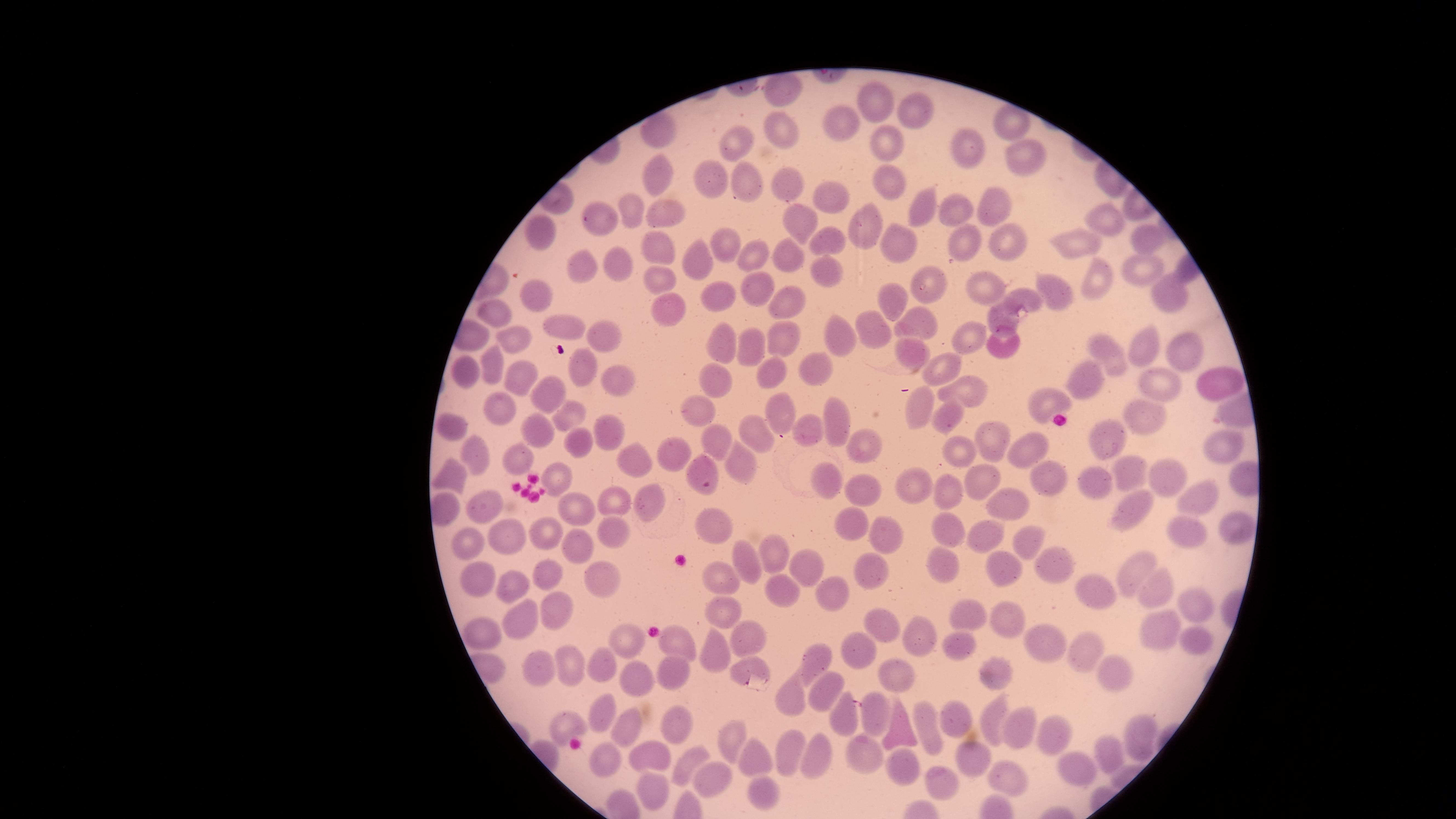

stain = Giemsa
field of view = single
visible region = circular
capture = smartphone photograph through the microscope eyepiece
uninfected RBCs = approximate marker points, in pixels from the top-left corner: (x=782, y=91), (x=879, y=101), (x=919, y=115), (x=838, y=119), (x=782, y=128), (x=655, y=132), (x=963, y=138), (x=733, y=140), (x=886, y=141), (x=1022, y=149), (x=653, y=174), (x=712, y=177), (x=888, y=178), (x=753, y=180), (x=785, y=180), (x=830, y=198), (x=994, y=202), (x=622, y=204), (x=916, y=205), (x=658, y=209), (x=795, y=212), (x=958, y=214), (x=1103, y=217), (x=598, y=219), (x=871, y=226), (x=830, y=230), (x=1145, y=235), (x=1010, y=236), (x=542, y=237), (x=896, y=238), (x=1078, y=240), (x=724, y=242), (x=958, y=246), (x=662, y=248), (x=702, y=254), (x=754, y=254), (x=794, y=254), (x=584, y=262), (x=830, y=262), (x=618, y=263), (x=1146, y=266), (x=664, y=278), (x=1103, y=278), (x=929, y=282), (x=982, y=286), (x=760, y=287), (x=1050, y=289), (x=894, y=291), (x=720, y=293), (x=545, y=294), (x=1179, y=298), (x=1026, y=299), (x=788, y=302), (x=664, y=304), (x=495, y=316), (x=917, y=316), (x=1004, y=319), (x=869, y=321), (x=568, y=326), (x=602, y=335), (x=963, y=336), (x=786, y=338), (x=516, y=340), (x=730, y=341), (x=841, y=341), (x=1004, y=342), (x=753, y=343), (x=908, y=344), (x=1182, y=345), (x=1149, y=349), (x=491, y=355), (x=1108, y=358), (x=579, y=365), (x=943, y=366), (x=822, y=367), (x=771, y=368), (x=469, y=374), (x=607, y=378), (x=1085, y=379), (x=1213, y=379), (x=718, y=383), (x=521, y=385), (x=969, y=386), (x=1159, y=386), (x=553, y=397), (x=1041, y=398), (x=780, y=405), (x=921, y=405), (x=699, y=406), (x=502, y=410), (x=572, y=414), (x=1141, y=418), (x=830, y=419), (x=948, y=421), (x=452, y=429), (x=537, y=430), (x=613, y=430), (x=813, y=432), (x=714, y=435), (x=994, y=435), (x=756, y=436), (x=1225, y=439), (x=579, y=441), (x=1106, y=441), (x=1023, y=445), (x=969, y=449), (x=517, y=450), (x=867, y=450), (x=677, y=451), (x=634, y=458), (x=479, y=459), (x=745, y=459), (x=705, y=465), (x=1055, y=471), (x=1136, y=472), (x=560, y=476), (x=455, y=478), (x=1178, y=478), (x=834, y=483), (x=989, y=483), (x=1102, y=483), (x=913, y=491), (x=858, y=493), (x=949, y=493), (x=1200, y=496), (x=649, y=500), (x=1004, y=502), (x=620, y=504), (x=486, y=508), (x=1137, y=509), (x=443, y=510), (x=580, y=514), (x=857, y=520), (x=712, y=522), (x=943, y=528), (x=619, y=529), (x=890, y=529), (x=1235, y=529), (x=546, y=531), (x=1188, y=533), (x=506, y=536), (x=988, y=537), (x=1030, y=540), (x=578, y=545), (x=470, y=547), (x=774, y=548), (x=943, y=561), (x=807, y=563), (x=1056, y=563), (x=752, y=566), (x=876, y=568), (x=1001, y=569), (x=1140, y=570), (x=546, y=578), (x=481, y=581), (x=511, y=581), (x=604, y=581), (x=725, y=585), (x=831, y=588), (x=785, y=591), (x=1099, y=592), (x=1161, y=594), (x=553, y=600), (x=1194, y=603), (x=974, y=611), (x=525, y=613), (x=723, y=614), (x=1010, y=620), (x=879, y=625), (x=487, y=631), (x=917, y=631), (x=1165, y=632), (x=679, y=639), (x=749, y=639), (x=1044, y=641), (x=627, y=642), (x=854, y=644), (x=1203, y=645), (x=956, y=651), (x=710, y=652), (x=1089, y=655), (x=819, y=660), (x=567, y=663), (x=606, y=664), (x=677, y=666), (x=743, y=670), (x=543, y=671), (x=1001, y=671), (x=897, y=673), (x=1115, y=673), (x=631, y=679), (x=824, y=690), (x=791, y=695), (x=605, y=708), (x=958, y=713), (x=992, y=715), (x=843, y=716), (x=877, y=719), (x=675, y=720), (x=562, y=721), (x=928, y=727), (x=900, y=728), (x=1023, y=729), (x=621, y=730), (x=734, y=734), (x=1053, y=737), (x=1140, y=740), (x=864, y=751), (x=748, y=753), (x=788, y=756), (x=648, y=757), (x=1108, y=757), (x=819, y=758), (x=976, y=758), (x=606, y=762), (x=690, y=762), (x=901, y=771), (x=1010, y=776), (x=1081, y=776), (x=716, y=780), (x=937, y=780), (x=649, y=790), (x=759, y=793)
preparation = thin smear of blood
image size = 1456×819 pixels
presence = no malaria parasites detected